Assess this cell for malaria.
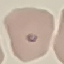

It is parasitized.

Summary:
  - Image type: automatically extracted cell patch, resized to 64 × 64 pixels
  - Capture: smartphone through the microscope eyepiece
  - Stain: Giemsa
  - Preparation: thin smear